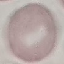
Summary:
  - Malaria status: uninfected
  - Stain: Giemsa
  - Preparation: thin blood smear
  - Capture: smartphone through the microscope eyepiece
  - Image type: cell patch, automatically extracted from a larger field of view and resized to 64 × 64 pixels